Classify this cell by malaria status.
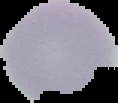

It is uninfected.

From a thin blood smear. Image is 118×103 pixels. The area outside the segmented cell region is set to black.